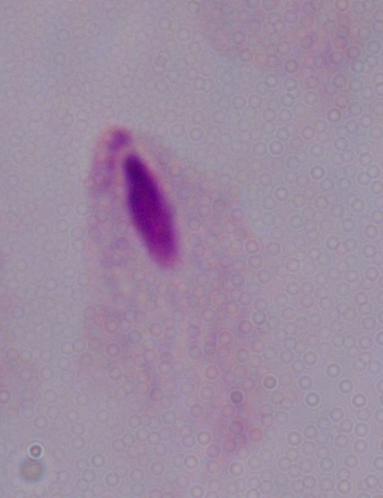
Summary:
  - Magnification: 1000x
  - Modality: photomicrograph
  - Identification: trichomonad